Comment on the morphology of the erythrocytes.
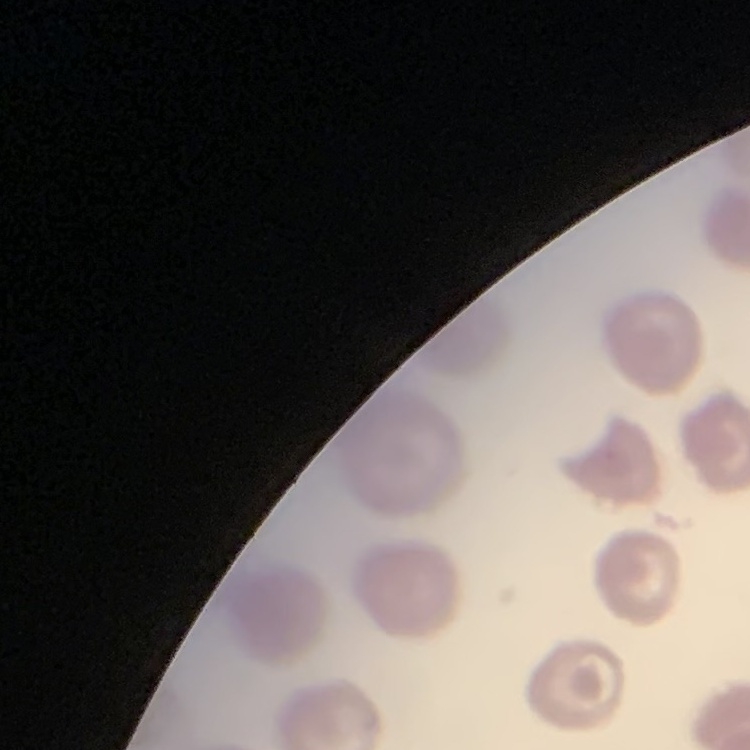

No rouleaux formation.

Summary:
  - Image type: one tile cut from a larger photomicrograph
  - Preparation: thin blood film
  - Stain: Field's or Giemsa